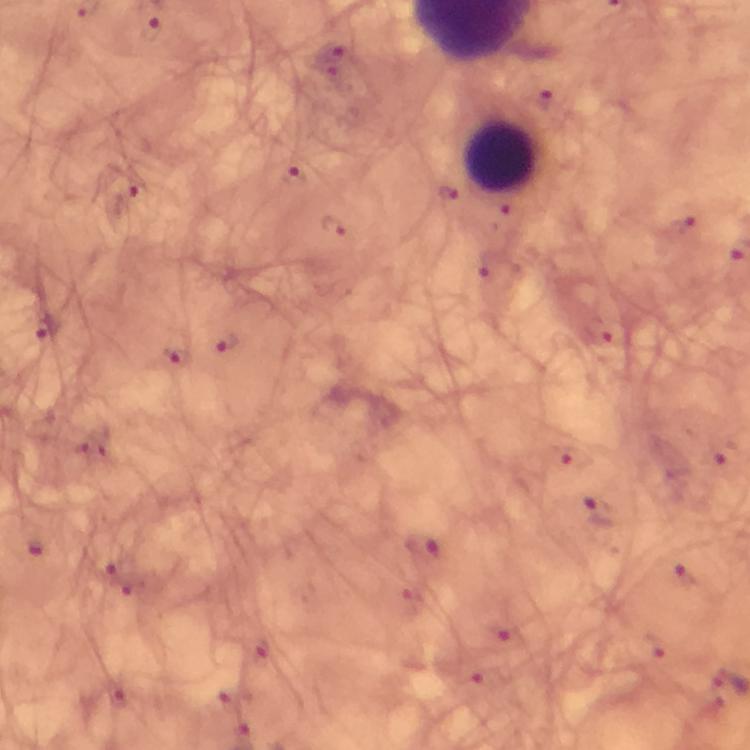

Approximate centers as [x, y] in pixels. Plasmodium parasite locations: [151, 31], [334, 64], [293, 180], [449, 196], [683, 224], [333, 226], [494, 268], [46, 330], [597, 333], [227, 341], [174, 358], [596, 516], [36, 547], [420, 548], [685, 574], [498, 634]. Leukocyte locations: [502, 159]. From a malaria diagnostic workup. 100x magnification. Photographed with a smartphone mounted on the microscope. Immersion oil applied. Thick blood film. Cropped region of a single field of view. Giemsa-stained preparation. Image is 750×750 pixels.